Evaluate for Plasmodium parasites.
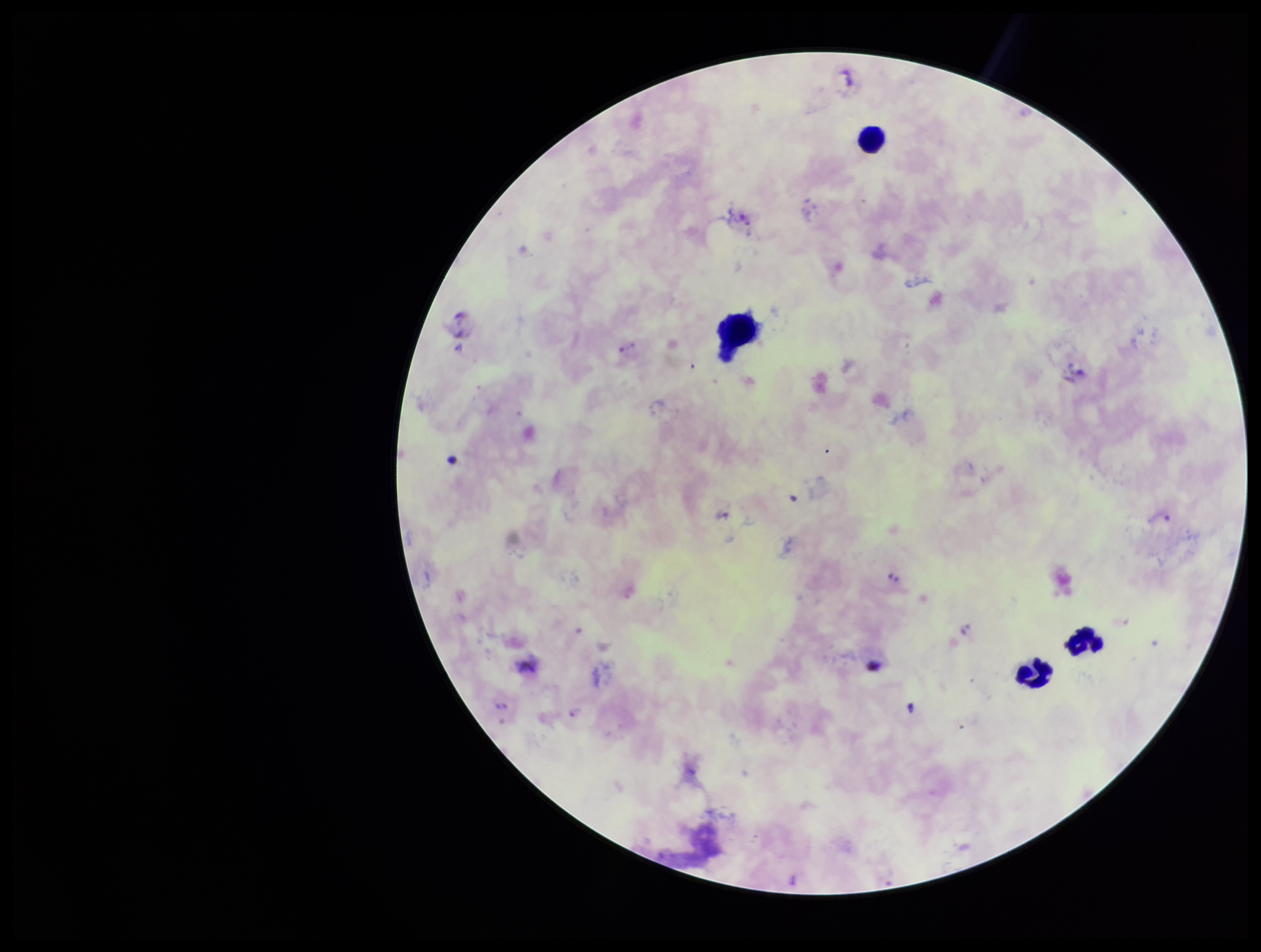

Identified.

parasite count = 7
stain = Giemsa
image size = 1261×952 pixels
patient malaria status = positive
leukocyte count = 4
field of view = single
species reported for this patient = Plasmodium vivax
capture = smartphone photograph through the microscope eyepiece
preparation = thick